Evaluate for malaria.
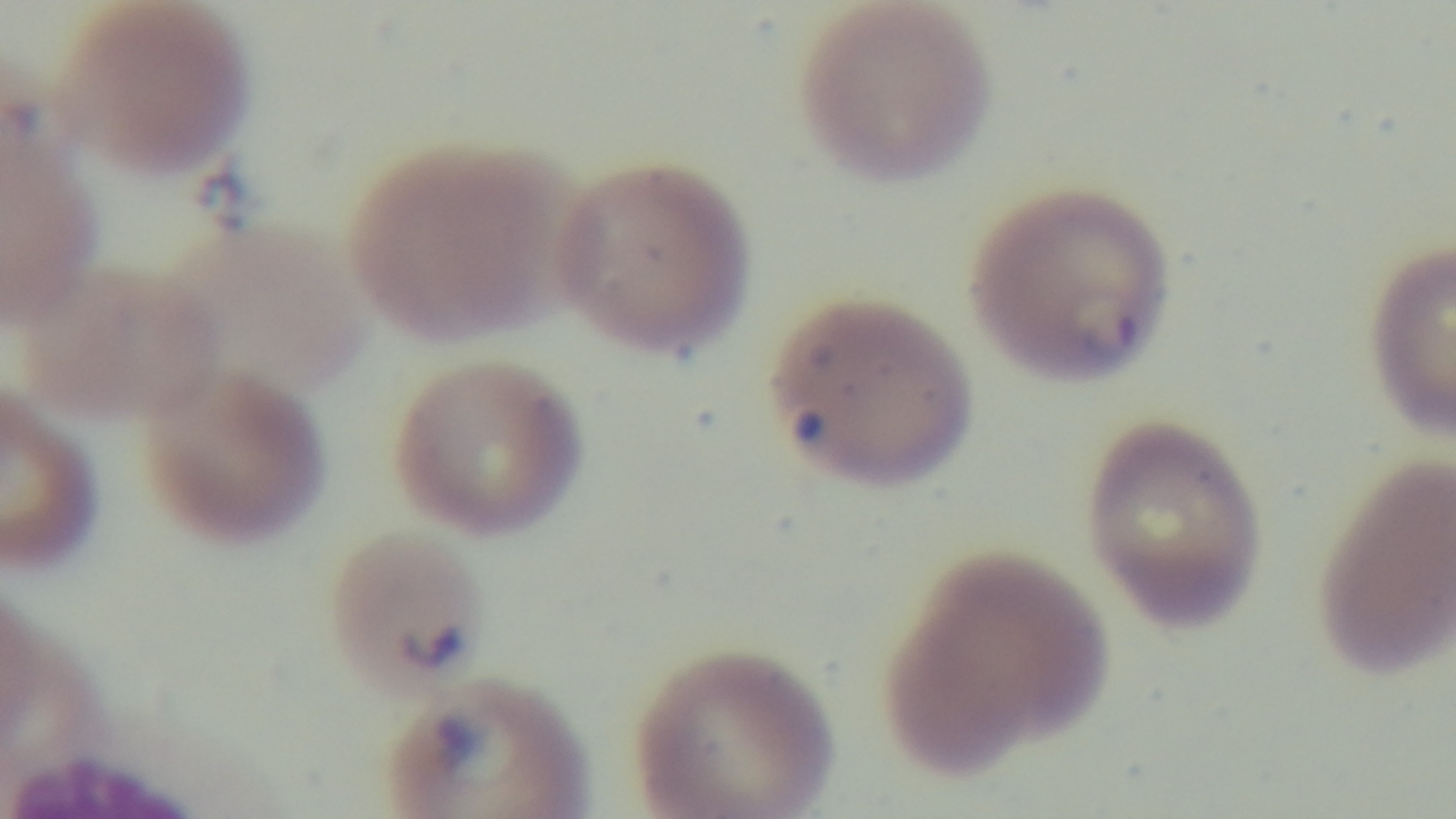
Positive.

capture = mounted 4K digital camera
stain = Giemsa
modality = light microscopy
field of view = single
objective = 100x oil immersion
preparation = thin